Identify the parasite.
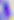

Toxoplasma gondii.

Micrograph. Captured at 400x magnification.